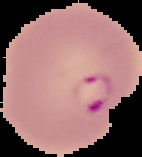
Summary:
  - Preparation: thin blood film
  - Image size: 142×157 pixels
  - Image type: segmented cell region on a black background
  - Malaria status: parasitized